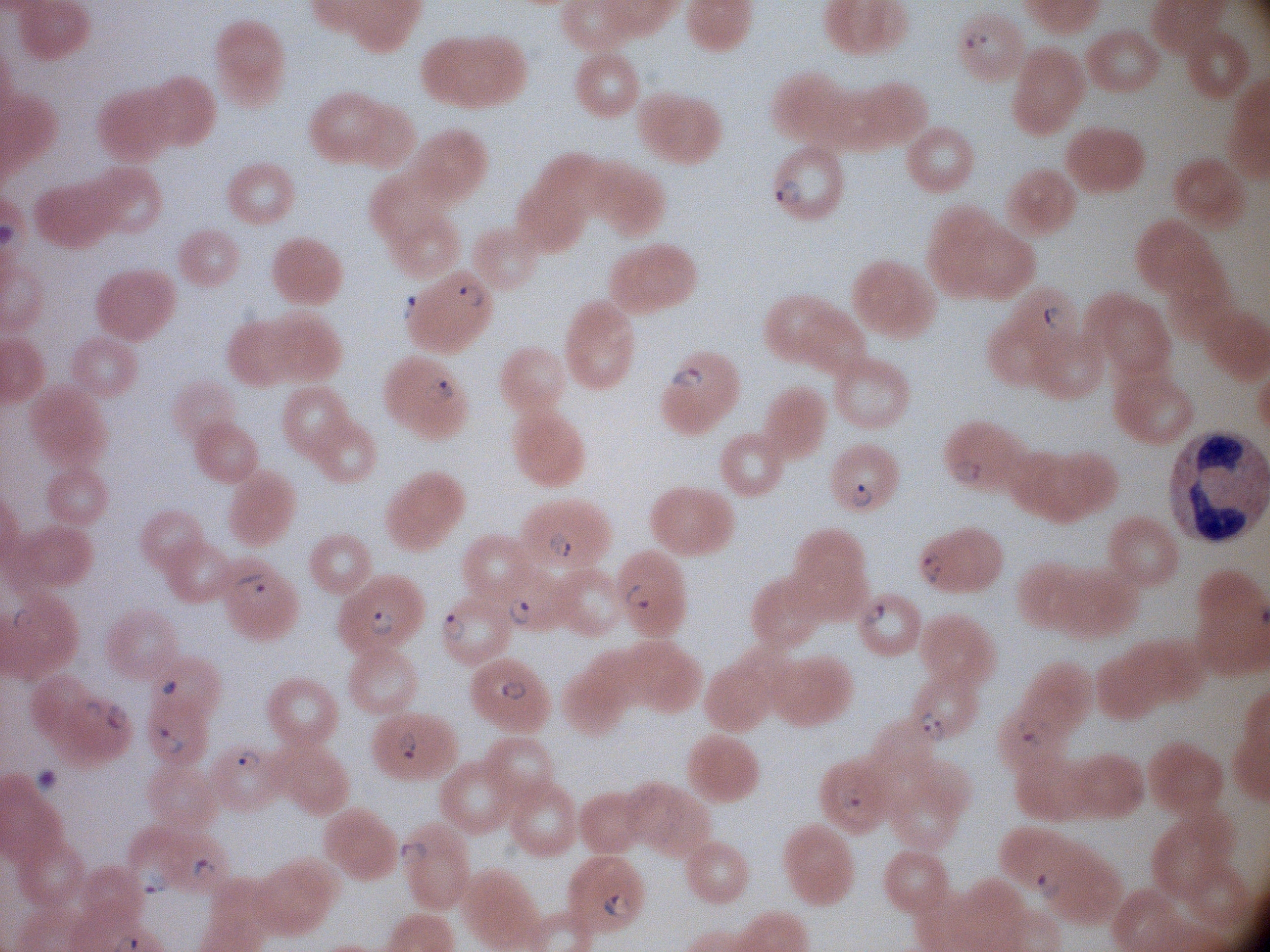 Approximate bounding boxes as named x1/y1/x2/y2 corners in pixels, from the source annotation, which is not necessarily exhaustive. Ring form locations: (x1=956, y1=28, x2=995, y2=55), (x1=773, y1=177, x2=805, y2=207), (x1=454, y1=282, x2=486, y2=310), (x1=399, y1=293, x2=421, y2=324), (x1=1040, y1=304, x2=1068, y2=330), (x1=670, y1=364, x2=708, y2=391), (x1=422, y1=374, x2=457, y2=404), (x1=950, y1=456, x2=985, y2=485), (x1=849, y1=483, x2=875, y2=511), (x1=544, y1=532, x2=575, y2=560), (x1=916, y1=551, x2=945, y2=586), (x1=235, y1=569, x2=272, y2=604), (x1=621, y1=580, x2=652, y2=613), (x1=507, y1=595, x2=535, y2=628), (x1=859, y1=599, x2=887, y2=628), (x1=9, y1=606, x2=33, y2=633), (x1=366, y1=607, x2=400, y2=640), (x1=437, y1=613, x2=470, y2=643), (x1=499, y1=677, x2=529, y2=703), (x1=82, y1=700, x2=103, y2=722), (x1=101, y1=703, x2=131, y2=732), (x1=916, y1=708, x2=949, y2=744), (x1=1016, y1=715, x2=1054, y2=750), (x1=153, y1=726, x2=187, y2=756), (x1=395, y1=726, x2=421, y2=762), (x1=232, y1=745, x2=263, y2=773), (x1=836, y1=785, x2=868, y2=812), (x1=395, y1=839, x2=428, y2=867), (x1=190, y1=857, x2=218, y2=883), (x1=137, y1=864, x2=173, y2=898), (x1=1035, y1=869, x2=1066, y2=902). Thin blood smear. Acquired with a Leica DM2000 optical microscope and its built-in camera. Giemsa stain. 100x magnification. Image is 1270×952 pixels. One field from this slide. Species: Plasmodium falciparum.